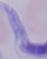
magnification: 1000x
identification: trypanosome
modality: photomicrograph